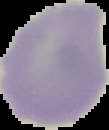

Summary:
  - Preparation: thin blood smear
  - Malaria status: uninfected
  - Image size: 109×130 pixels
  - Image type: segmented cell region with the area outside set to black